Report the malaria status of this cell.
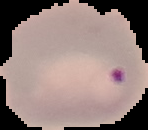

It is parasitized.

From a thin blood smear. Cell region segmented out of the field of view; the surrounding area is masked to black. Image is 148×130 pixels.